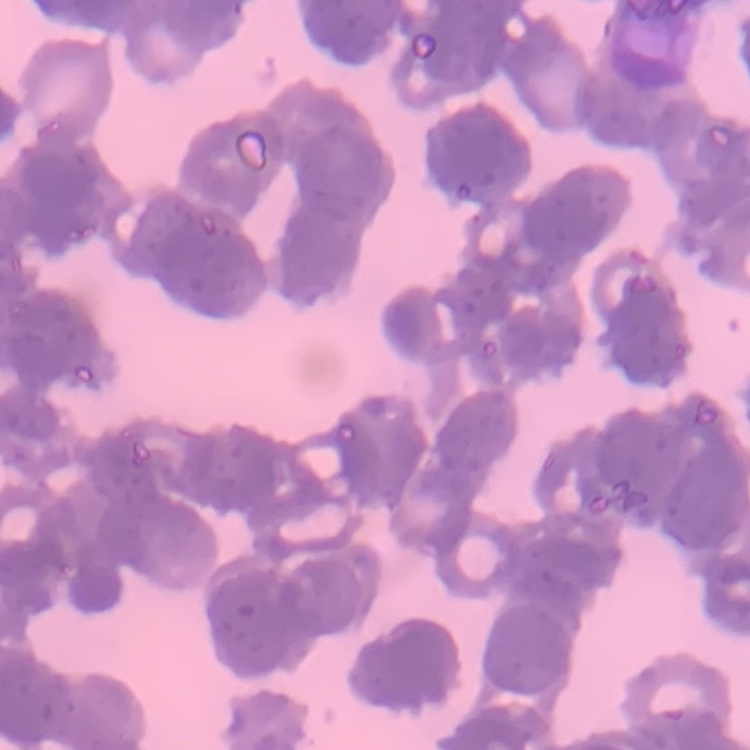 The erythrocytes show rouleaux formation. Thin blood film. One tile cut from a larger photomicrograph. Stained with either Field's or Giemsa.